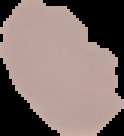
malaria_status: parasitized
image_type: cell region segmented out of the field of view; surrounding area masked to black
preparation: thin blood smear
image_size: 124×136 pixels